Assess the morphology of the erythrocytes.
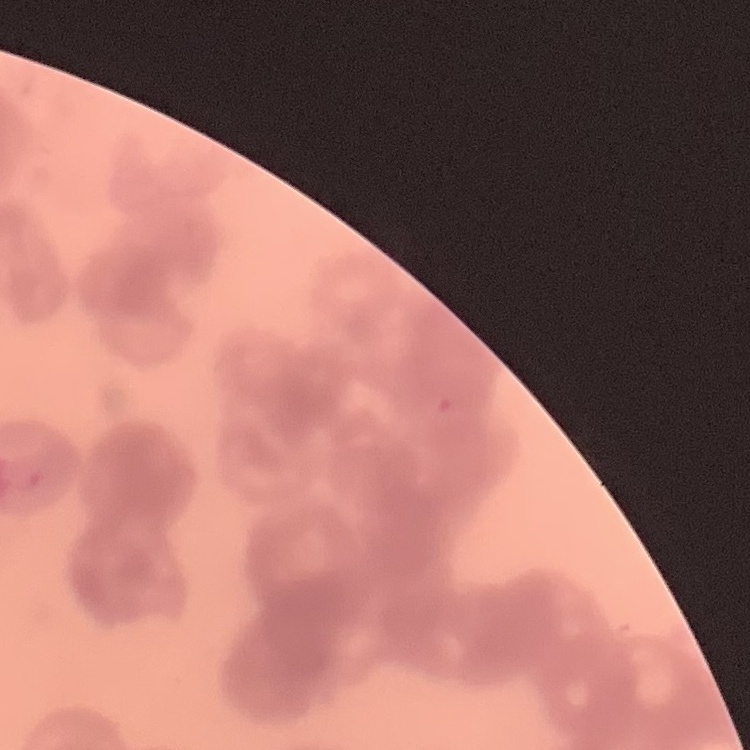

They show rouleaux formation.

image type = one tile cut from a larger photomicrograph
preparation = thin blood film
stain = Field's or Giemsa